Classify this cell by malaria status.
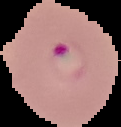
Parasitized.

Cell region segmented out of the field of view; the surrounding area is masked to black. From a thin blood smear. Image is 121×127 pixels.